Outline each blood parasite and name the species.
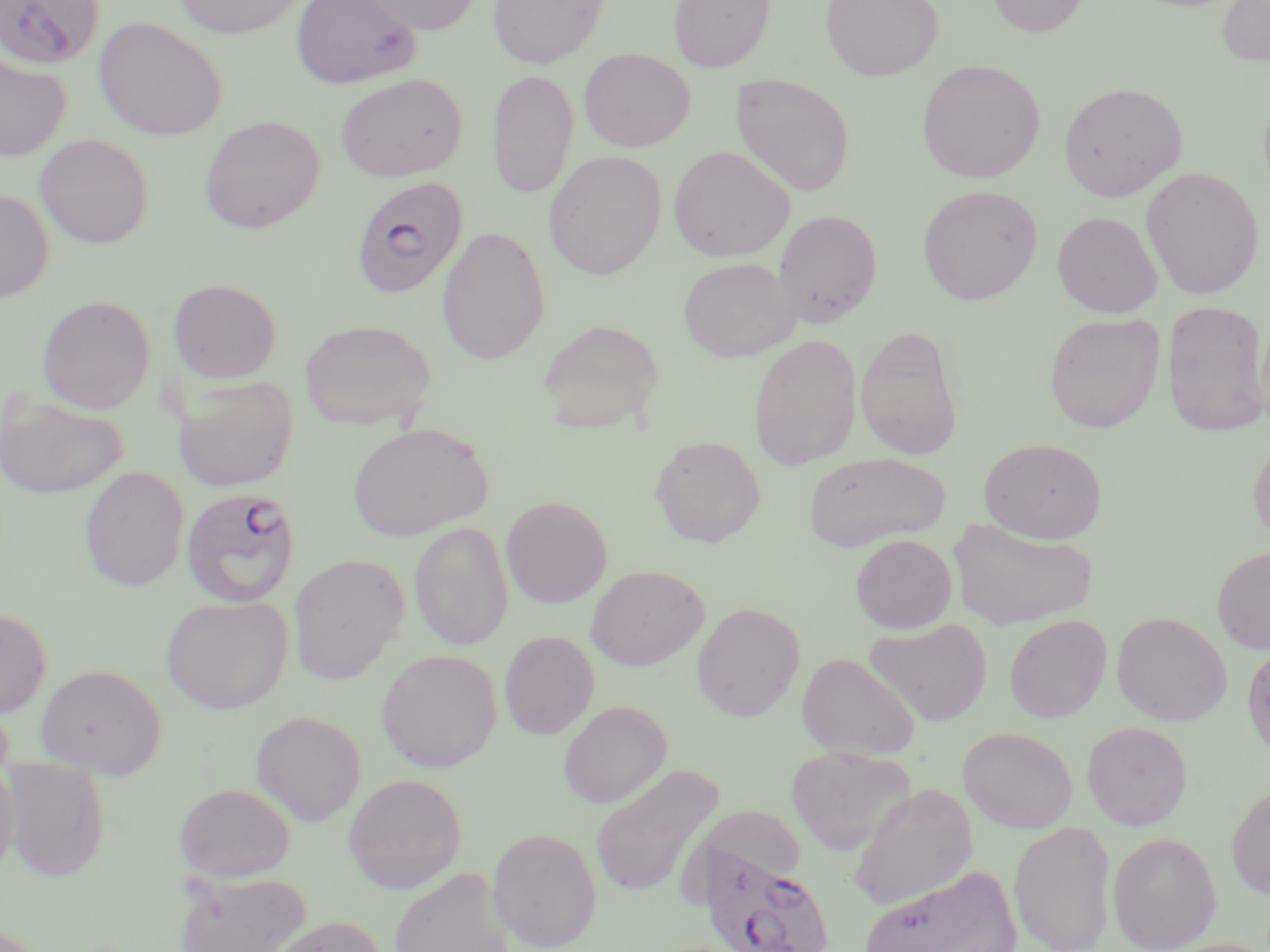

Approximate bounding boxes as (x1, y1, x2, y2) in pixels.
Plasmodium falciparum-infected red blood cells: (0, 0, 104, 70), (351, 175, 467, 298), (180, 486, 301, 608), (699, 840, 836, 952).
No Plasmodium ovale, Plasmodium malariae, Plasmodium vivax, Babesia divergens, or Trypanosoma brucei observed.

Summary:
  - Uninfected red blood cell locations: (174, 0, 310, 38), (290, 0, 421, 89), (355, 0, 482, 35), (487, 0, 608, 68), (668, 0, 775, 73), (821, 0, 943, 81), (987, 0, 1089, 37), (1217, 1, 1270, 66), (93, 17, 227, 140), (578, 48, 695, 152), (0, 52, 71, 162), (916, 60, 1045, 183), (486, 69, 579, 199), (334, 73, 468, 182), (730, 73, 855, 196), (1058, 82, 1188, 202), (199, 116, 324, 234), (34, 134, 153, 248), (668, 145, 795, 262), (543, 151, 666, 280), (1141, 166, 1265, 300), (918, 184, 1043, 305), (0, 189, 54, 301), (773, 209, 883, 327), (1052, 211, 1163, 318), (437, 226, 550, 365), (679, 257, 800, 361), (168, 279, 282, 383), (36, 295, 155, 414), (1161, 299, 1270, 437), (1045, 313, 1165, 433), (299, 319, 436, 431), (538, 319, 665, 432), (854, 326, 964, 459), (748, 334, 862, 470), (173, 376, 299, 492), (0, 391, 129, 500), (347, 421, 492, 542), (1248, 435, 1270, 547), (650, 436, 766, 547), (979, 438, 1107, 543), (803, 452, 949, 551), (80, 467, 189, 591), (501, 496, 612, 608), (947, 519, 1099, 630), (409, 522, 513, 651), (850, 534, 957, 634), (1212, 545, 1270, 655), (288, 554, 408, 684), (586, 565, 709, 671), (161, 596, 292, 713), (691, 603, 805, 722), (0, 608, 52, 718), (1111, 612, 1232, 726), (1004, 614, 1112, 723), (864, 618, 993, 727), (499, 631, 600, 739), (1241, 642, 1270, 763), (376, 650, 502, 773), (797, 652, 919, 760), (35, 663, 166, 777), (558, 700, 671, 808), (250, 710, 367, 826), (1082, 721, 1193, 830), (958, 727, 1078, 833), (785, 746, 915, 855), (0, 755, 19, 881), (2, 758, 111, 882), (590, 763, 723, 900), (343, 773, 466, 893), (175, 782, 296, 881), (1225, 782, 1270, 900), (847, 784, 978, 912), (679, 811, 806, 913), (1009, 820, 1116, 952), (487, 827, 602, 951), (1107, 832, 1222, 951), (860, 865, 1022, 951), (389, 867, 516, 952), (175, 870, 312, 952), (266, 915, 387, 952)
  - Slide-level diagnosis: Plasmodium falciparum
  - Modality: light microscopy
  - Preparation: thin blood film
  - Field of view: one of a larger specimen
  - Image size: 1270×952 pixels
  - Magnification: 1000x
  - Stain: May-Grünwald-Giemsa